Locate every leukocyte (white blood cell).
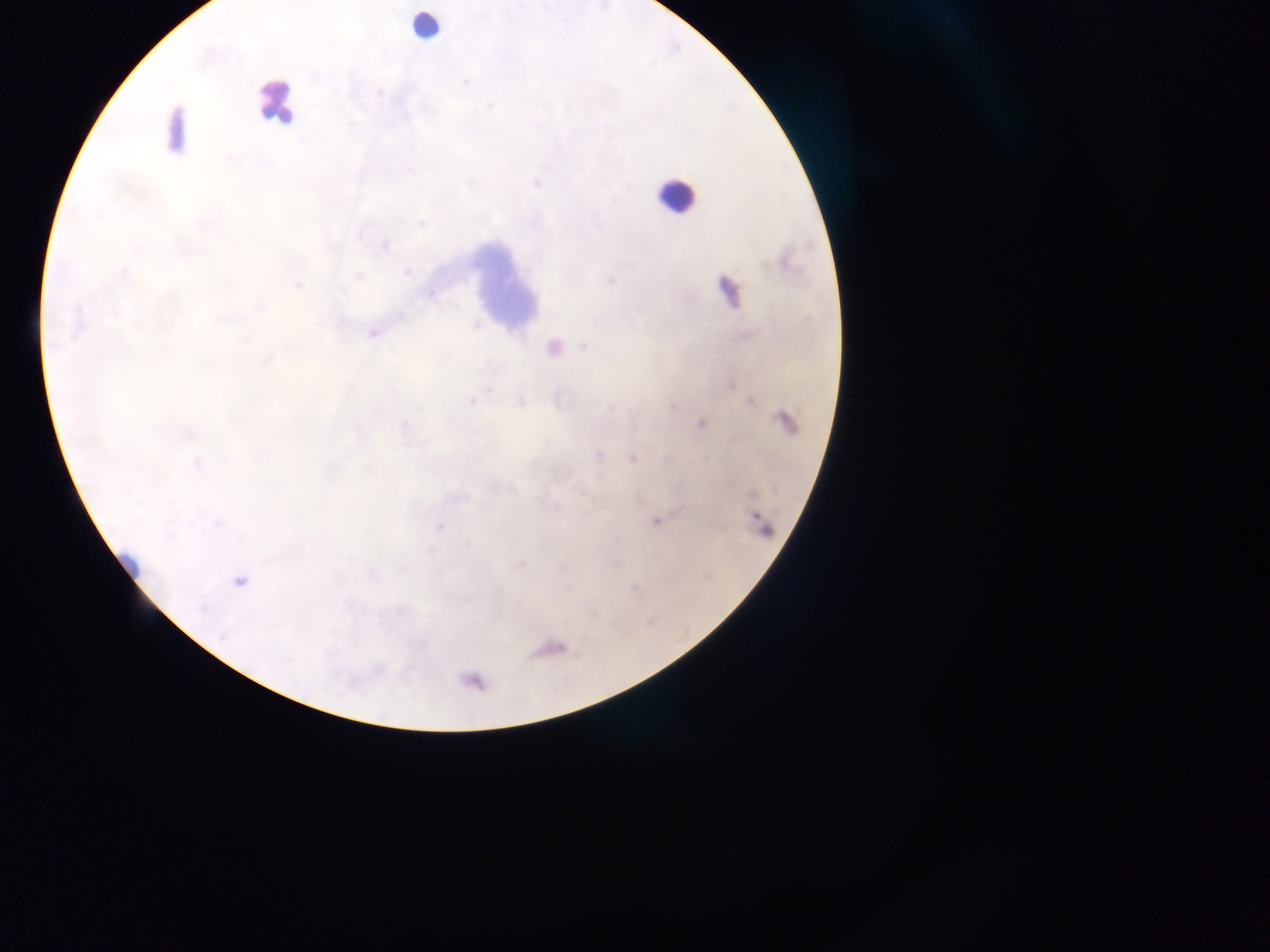
Approximate centers as {x, y} in pixels.
Leukocytes: {425, 25}, {276, 102}, {174, 130}, {674, 195}, {508, 286}.

field of view = single
malaria parasite locations = approximate centers as {x, y} in pixels: {378, 92}, {124, 272}, {298, 286}, {584, 347}, {471, 402}, {519, 402}, {701, 423}, {189, 435}, {598, 455}, {633, 458}, {196, 464}, {655, 521}, {239, 581}, {202, 609}
preparation = thick blood smear
capture = mobile-phone photograph through a microscope
country = Ghana
image size = 1270×952 pixels